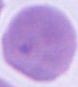

modality = micrograph
identification = red blood cell
magnification = 1000x